Describe the morphology of the erythrocytes.
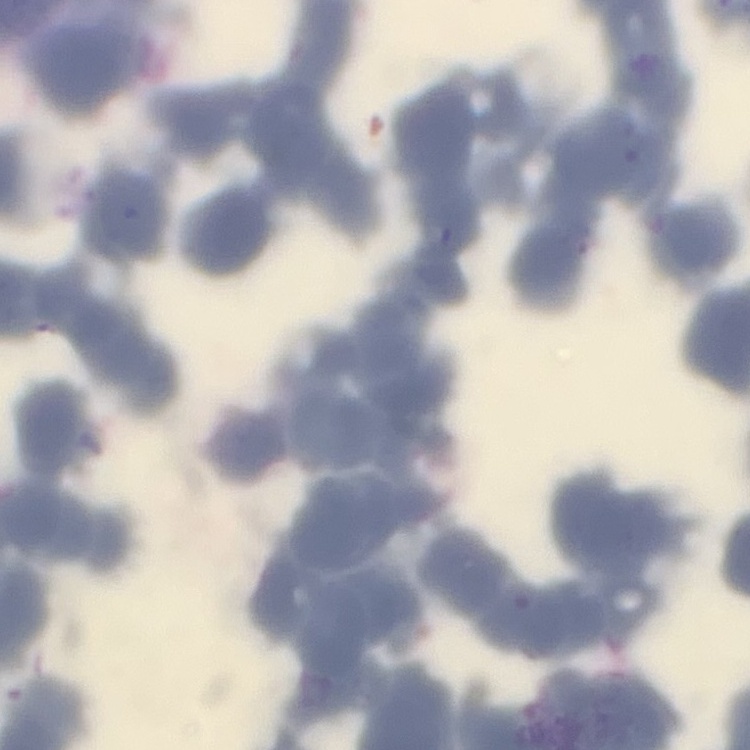

Rouleaux formation.

preparation = thin peripheral smear
stain = Field's or Giemsa
image type = one tile cut from a larger photomicrograph